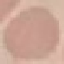
malaria status = uninfected
image type = automatically extracted cell patch, resized to 64 × 64 pixels
stain = Giemsa
preparation = thin blood smear
capture = smartphone camera at the microscope eyepiece